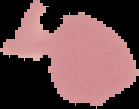 From a thin blood film. Malaria status: uninfected. Image is 139×109 pixels. Segmented cell region on a black background.